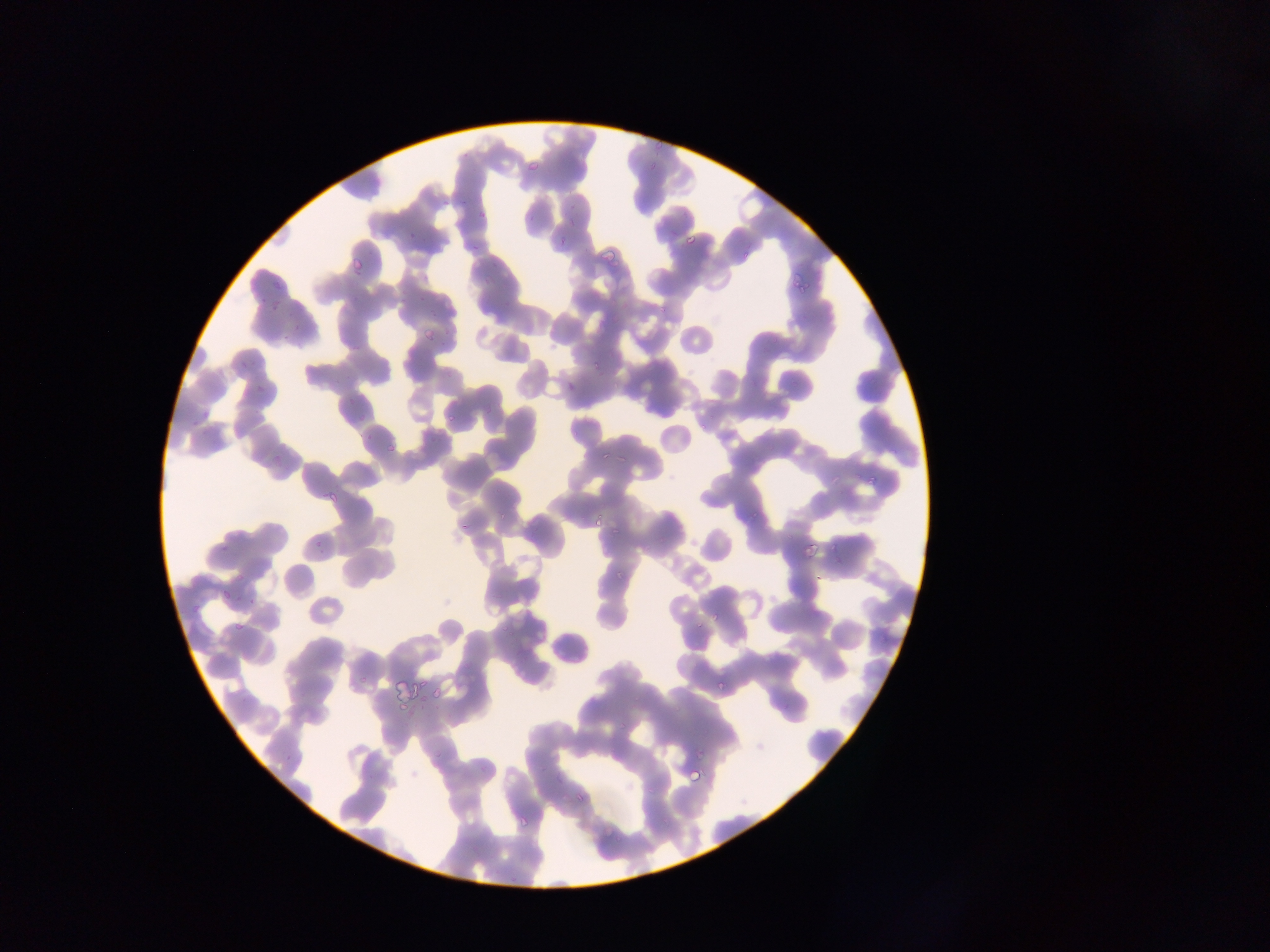

plasmodium_parasite_locations: 'approximate bounding boxes as {left, top, right, bottom} in pixels: {524, 154, 544, 175}, {645, 156, 659, 172}, {404, 219, 418, 240}, {683, 227, 704, 246}, {553, 234, 569, 250}, {594, 238, 621, 259}, {463, 241, 487, 252}, {352, 253, 360, 279}, {794, 277, 810, 295}, {273, 282, 284, 301}, {250, 287, 263, 313}, {424, 329, 438, 344}, {561, 373, 579, 390}, {442, 411, 455, 431}, {384, 443, 396, 457}, {596, 447, 612, 460}, {864, 462, 882, 487}, {327, 491, 342, 507}, {593, 508, 610, 534}, {609, 525, 625, 538}, {801, 542, 818, 559}, {827, 544, 842, 552}, {613, 562, 626, 578}, {218, 583, 232, 603}, {712, 611, 725, 623}, {230, 618, 245, 634}, {689, 619, 701, 631}, {709, 679, 723, 696}, {435, 693, 444, 703}, {692, 747, 704, 762}, {684, 762, 707, 787}, {569, 788, 590, 800}, {516, 811, 533, 830}'
country: Ghana
capture: mobile-phone photograph through a microscope
field_of_view: single
preparation: thin blood smear
image_size: 1270×952 pixels